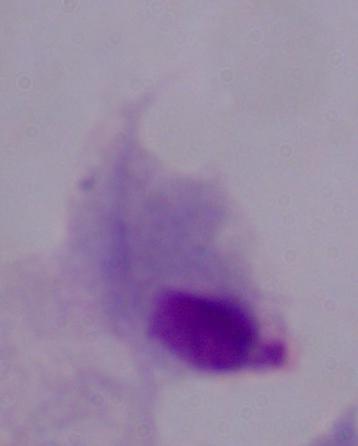

modality: photomicrograph
magnification: 1000x
identification: trichomonad